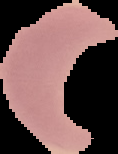

Summary:
  - Malaria status: uninfected
  - Image type: segmented cell region with the area outside set to black
  - Preparation: thin blood film
  - Image size: 118×154 pixels